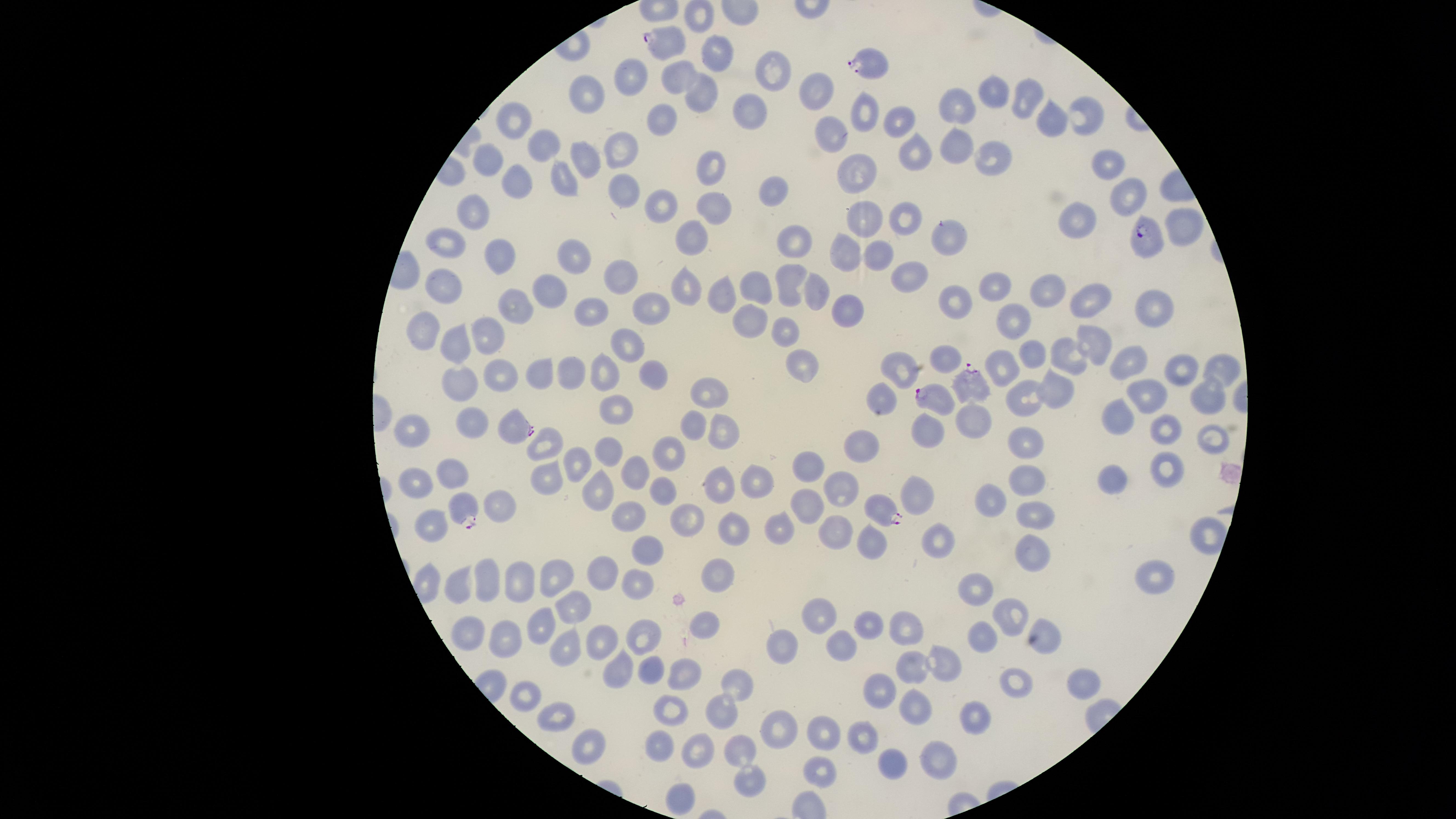
Approximate marker points, in pixels from the top-left corner. Uninfected red blood cells: (x=715, y=54), (x=637, y=72), (x=684, y=73), (x=767, y=77), (x=815, y=92), (x=701, y=93), (x=995, y=93), (x=583, y=95), (x=1028, y=99), (x=958, y=107), (x=749, y=112), (x=864, y=112), (x=1086, y=114), (x=663, y=115), (x=515, y=120), (x=895, y=120), (x=1050, y=122), (x=832, y=134), (x=546, y=140), (x=956, y=144), (x=624, y=150), (x=912, y=152), (x=989, y=154), (x=492, y=156), (x=585, y=159), (x=1108, y=164), (x=712, y=166), (x=853, y=174), (x=565, y=179), (x=519, y=180), (x=627, y=192), (x=773, y=192), (x=1127, y=194), (x=660, y=199), (x=469, y=207), (x=717, y=210), (x=864, y=217), (x=905, y=217), (x=1079, y=221), (x=1187, y=225), (x=689, y=236), (x=952, y=238), (x=450, y=240), (x=791, y=242), (x=852, y=249), (x=880, y=251), (x=504, y=252), (x=575, y=258), (x=623, y=271), (x=907, y=276), (x=786, y=281), (x=691, y=283), (x=749, y=287), (x=442, y=290), (x=815, y=290), (x=546, y=293), (x=999, y=293), (x=720, y=295), (x=1051, y=295), (x=1093, y=300), (x=954, y=302), (x=516, y=305), (x=650, y=305), (x=851, y=306), (x=1149, y=307), (x=589, y=310), (x=753, y=317), (x=1012, y=322), (x=784, y=328), (x=423, y=331), (x=458, y=337), (x=490, y=340), (x=631, y=342), (x=1095, y=342), (x=1032, y=353), (x=948, y=356), (x=1067, y=357), (x=799, y=359), (x=1130, y=360), (x=1221, y=367), (x=899, y=368), (x=1003, y=369), (x=458, y=370), (x=1177, y=370), (x=601, y=372), (x=575, y=373), (x=503, y=375), (x=540, y=375), (x=654, y=376), (x=1209, y=389), (x=1059, y=390), (x=711, y=392), (x=884, y=396), (x=1148, y=396), (x=1023, y=397), (x=622, y=402), (x=1116, y=414), (x=973, y=415), (x=475, y=421), (x=689, y=423), (x=716, y=427), (x=1163, y=427), (x=411, y=428), (x=931, y=429), (x=1214, y=435), (x=545, y=442), (x=863, y=442), (x=1026, y=446), (x=612, y=452), (x=672, y=454), (x=582, y=461), (x=1166, y=465), (x=809, y=469), (x=638, y=470), (x=456, y=473), (x=1028, y=479), (x=1113, y=479), (x=752, y=480), (x=417, y=482), (x=722, y=483), (x=666, y=489), (x=600, y=490), (x=839, y=490), (x=990, y=496), (x=919, y=497), (x=499, y=505), (x=809, y=508), (x=1036, y=513), (x=690, y=514), (x=632, y=517), (x=431, y=519), (x=731, y=526), (x=783, y=527), (x=836, y=532), (x=871, y=540), (x=940, y=543), (x=648, y=552), (x=1030, y=554), (x=605, y=573), (x=562, y=574), (x=719, y=575), (x=522, y=576), (x=1157, y=577), (x=491, y=580), (x=461, y=582), (x=639, y=586), (x=979, y=589), (x=572, y=601), (x=1009, y=613), (x=815, y=616), (x=542, y=620), (x=703, y=620), (x=868, y=621), (x=907, y=624), (x=465, y=628), (x=982, y=633), (x=643, y=634), (x=1043, y=635), (x=511, y=636), (x=782, y=641), (x=600, y=643), (x=839, y=643), (x=564, y=651), (x=945, y=663), (x=652, y=668), (x=915, y=668), (x=618, y=671), (x=688, y=673), (x=1080, y=678), (x=734, y=682), (x=1018, y=685), (x=886, y=689), (x=524, y=690), (x=916, y=704), (x=671, y=708), (x=720, y=716), (x=559, y=718), (x=975, y=720), (x=778, y=727), (x=821, y=733), (x=863, y=737), (x=589, y=739), (x=660, y=747), (x=742, y=751), (x=696, y=752), (x=936, y=762), (x=891, y=764), (x=819, y=772), (x=744, y=783), (x=680, y=795). Parasitized red blood cells: (x=666, y=43), (x=870, y=60), (x=1148, y=237), (x=969, y=381), (x=937, y=397), (x=514, y=427), (x=878, y=506), (x=464, y=508). Species: Plasmodium falciparum. Presence: malaria parasites seen. Thin smear of blood. Single field of view. Photographed with a smartphone camera through the microscope eyepiece. Giemsa stain. Image is 1456×819 pixels. The visible region is circular.